Report the malaria status of this cell.
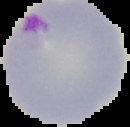

Parasitized.

From a thin blood film. The area outside the segmented cell region is set to black. Image is 130×127 pixels.